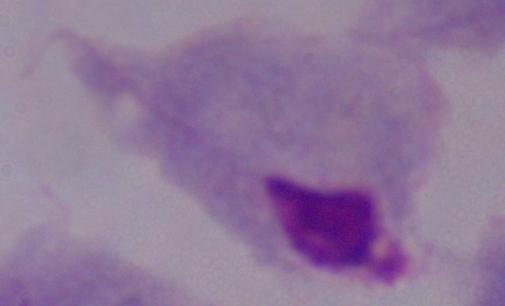

Summary:
  - Identification: trichomonad
  - Magnification: 1000x
  - Modality: micrograph